Assess the morphology of the erythrocytes.
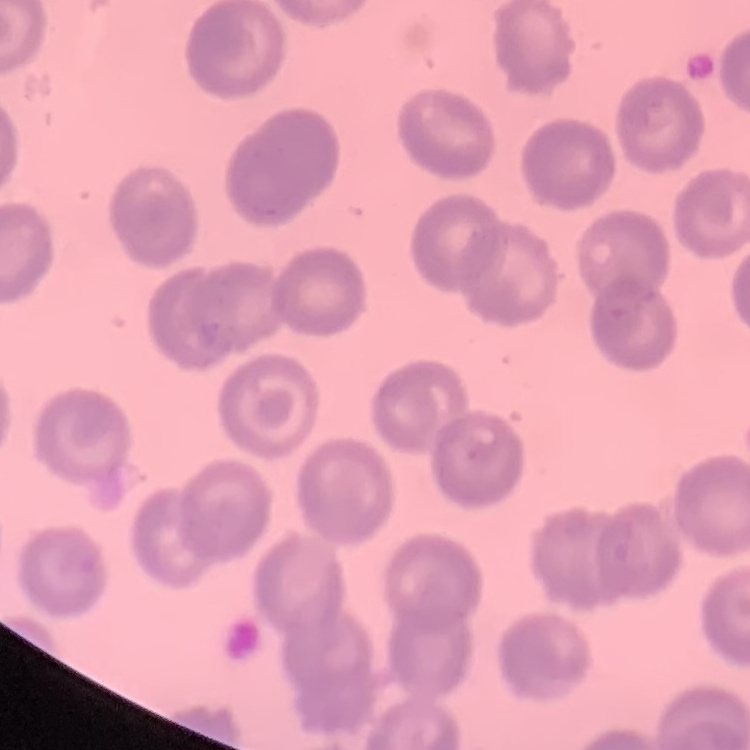
No rouleaux formation.

Summary:
  - Image type: one tile cut from a larger photomicrograph
  - Stain: Field's or Giemsa
  - Preparation: thin blood smear